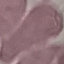

malaria status = uninfected
capture = smartphone camera at the microscope eyepiece
image type = automatically extracted cell patch, resized to 64 × 64 pixels
stain = Giemsa
preparation = thin blood film